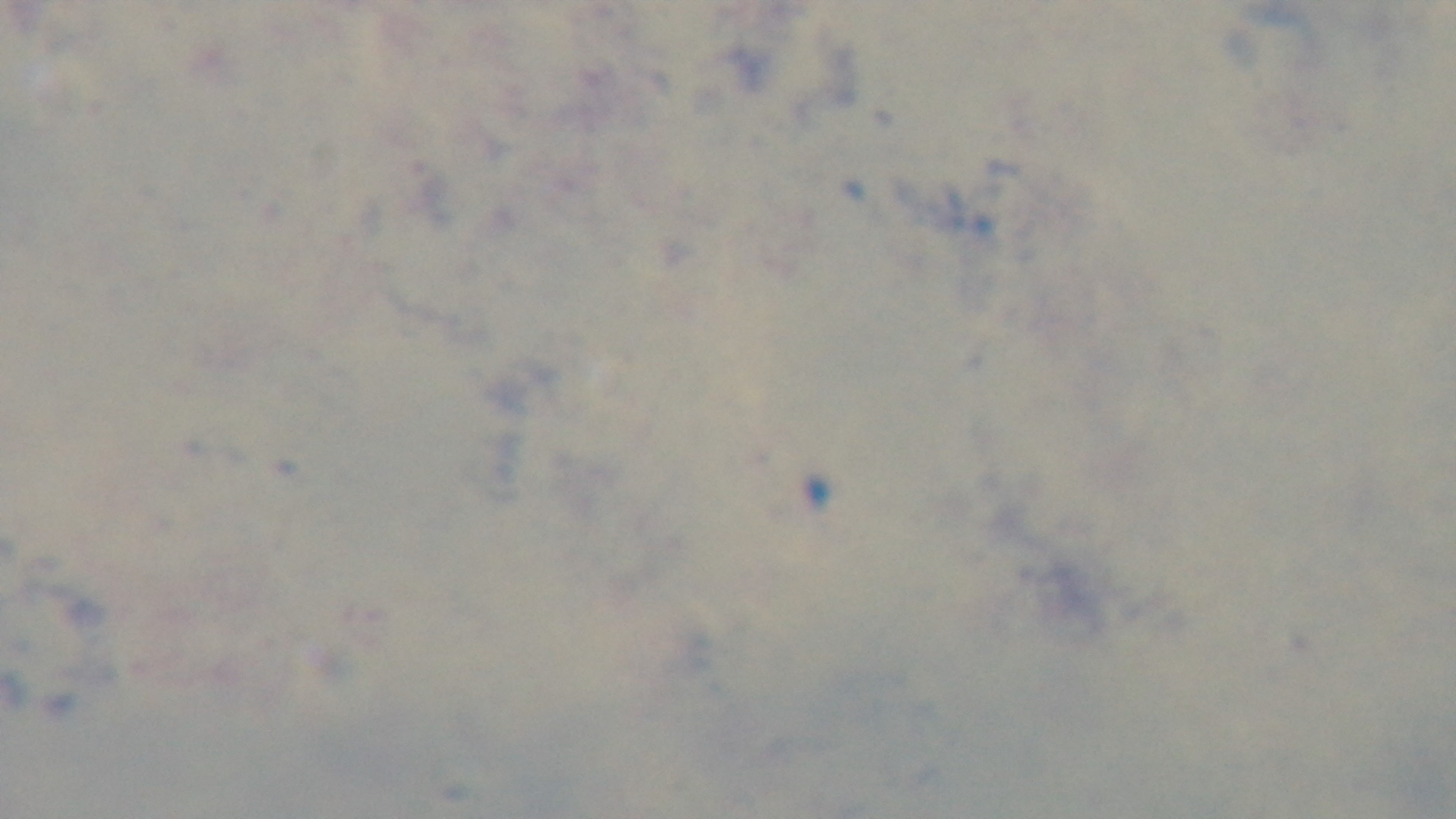

Summary:
  - Modality: light microscopy
  - Stain: Giemsa
  - Malaria status: uninfected
  - Preparation: thick
  - Objective: 100x oil immersion
  - Capture: mounted 4K digital camera
  - Field of view: single